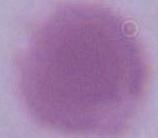
Micrograph. An erythrocyte is seen. Captured at 1000x magnification.